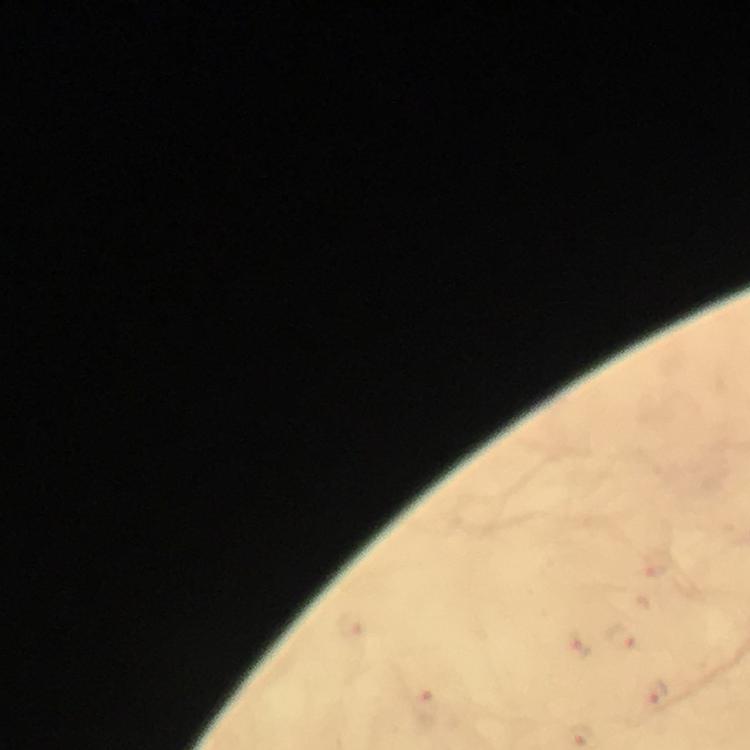

{
  "context": "from a diagnostic examination for malaria",
  "stain": "Giemsa",
  "cropped_from": "a single field of view",
  "magnification": "100x",
  "capture": "smartphone camera through the microscope",
  "malaria_parasite_locations": "approximate centers as {x, y} in pixels: {653, 560}, {626, 637}, {575, 644}, {658, 693}, {424, 707}, {584, 734}",
  "preparation": "thick smear",
  "image_size": "750×750 pixels",
  "immersion_oil": "applied"
}